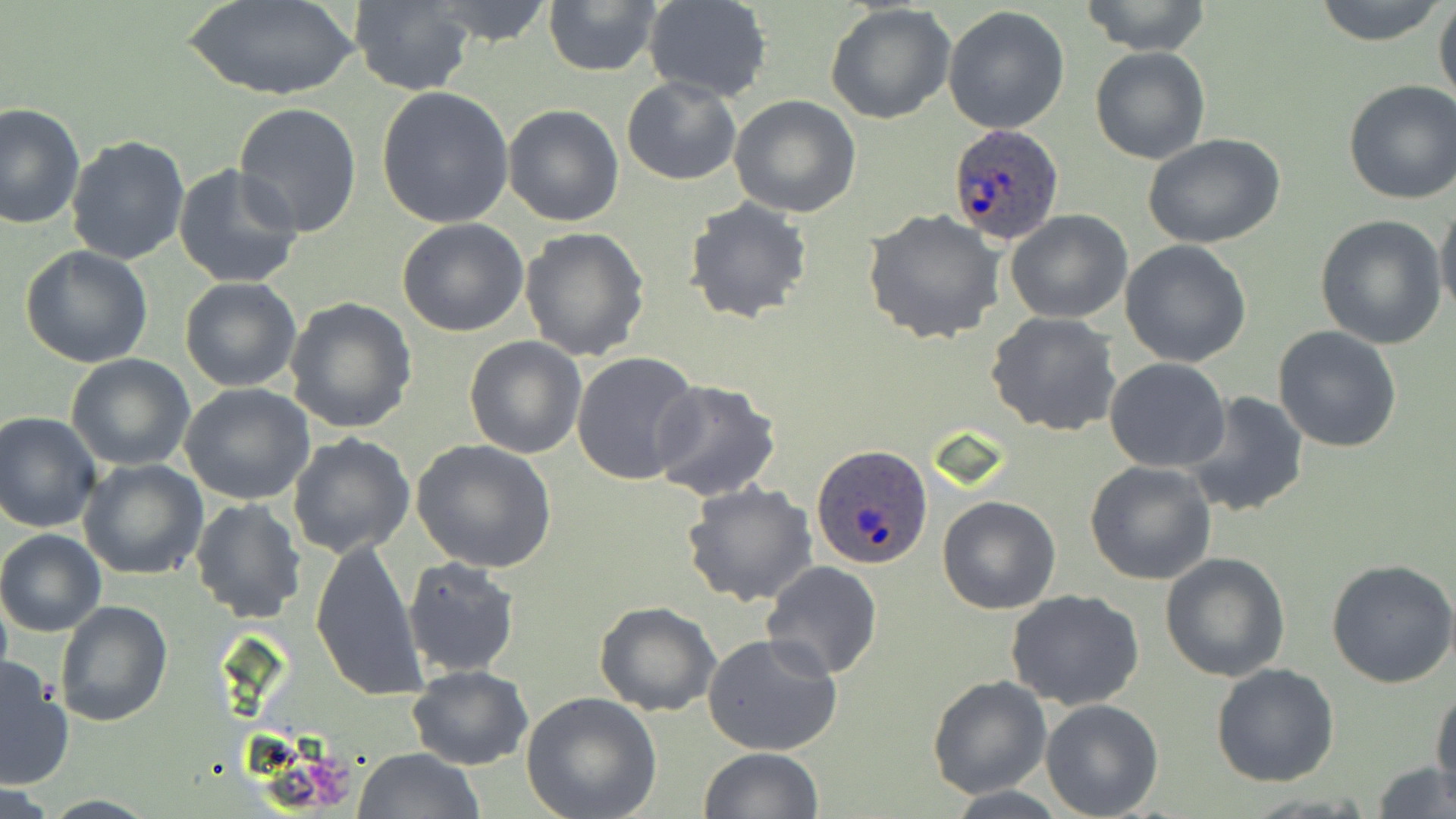 Approximate bounding boxes as named x1/y1/x2/y2 corners in pixels. Uninfected red blood cell locations: (x1=184, y1=0, x2=361, y2=102), (x1=424, y1=0, x2=557, y2=46), (x1=543, y1=0, x2=666, y2=76), (x1=644, y1=0, x2=773, y2=103), (x1=1312, y1=0, x2=1446, y2=45), (x1=1080, y1=1, x2=1211, y2=55), (x1=349, y1=2, x2=476, y2=94), (x1=1433, y1=2, x2=1456, y2=116), (x1=826, y1=3, x2=956, y2=125), (x1=943, y1=6, x2=1071, y2=134), (x1=1091, y1=46, x2=1211, y2=164), (x1=622, y1=76, x2=742, y2=186), (x1=1342, y1=80, x2=1456, y2=205), (x1=375, y1=87, x2=515, y2=231), (x1=729, y1=94, x2=861, y2=219), (x1=0, y1=102, x2=85, y2=232), (x1=232, y1=102, x2=363, y2=237), (x1=501, y1=103, x2=625, y2=226), (x1=1142, y1=133, x2=1286, y2=250), (x1=65, y1=134, x2=192, y2=266), (x1=172, y1=165, x2=303, y2=288), (x1=682, y1=198, x2=813, y2=324), (x1=1436, y1=199, x2=1455, y2=321), (x1=863, y1=209, x2=1003, y2=343), (x1=1005, y1=210, x2=1132, y2=325), (x1=1314, y1=216, x2=1448, y2=348), (x1=396, y1=218, x2=529, y2=337), (x1=519, y1=228, x2=651, y2=361), (x1=1120, y1=240, x2=1252, y2=368), (x1=19, y1=245, x2=153, y2=368), (x1=178, y1=277, x2=302, y2=392), (x1=285, y1=296, x2=417, y2=433), (x1=986, y1=310, x2=1122, y2=436), (x1=1272, y1=326, x2=1402, y2=451), (x1=464, y1=336, x2=585, y2=459), (x1=572, y1=350, x2=702, y2=487), (x1=66, y1=354, x2=196, y2=471), (x1=1105, y1=358, x2=1232, y2=472), (x1=648, y1=380, x2=781, y2=502), (x1=179, y1=383, x2=315, y2=504), (x1=1182, y1=391, x2=1309, y2=519), (x1=0, y1=412, x2=101, y2=533), (x1=287, y1=433, x2=416, y2=559), (x1=412, y1=440, x2=556, y2=574), (x1=78, y1=458, x2=207, y2=579), (x1=1085, y1=461, x2=1217, y2=586), (x1=681, y1=482, x2=820, y2=607), (x1=937, y1=495, x2=1060, y2=614), (x1=190, y1=499, x2=305, y2=621), (x1=0, y1=529, x2=105, y2=637), (x1=310, y1=540, x2=426, y2=701), (x1=1160, y1=553, x2=1292, y2=682), (x1=402, y1=557, x2=520, y2=679), (x1=1327, y1=557, x2=1456, y2=687), (x1=760, y1=560, x2=885, y2=679), (x1=1006, y1=591, x2=1146, y2=711), (x1=54, y1=600, x2=173, y2=727), (x1=596, y1=602, x2=720, y2=716), (x1=701, y1=632, x2=843, y2=755), (x1=0, y1=656, x2=74, y2=790), (x1=1211, y1=663, x2=1341, y2=787), (x1=407, y1=665, x2=534, y2=770), (x1=926, y1=675, x2=1051, y2=799), (x1=1432, y1=688, x2=1455, y2=798), (x1=520, y1=692, x2=663, y2=819), (x1=1040, y1=700, x2=1165, y2=818), (x1=354, y1=748, x2=483, y2=819), (x1=697, y1=748, x2=823, y2=819), (x1=1369, y1=762, x2=1453, y2=818). Plasmodium ovale-infected red blood cell locations: (x1=946, y1=123, x2=1064, y2=244), (x1=811, y1=444, x2=934, y2=572). Slide-level diagnosis: Plasmodium ovale. Single field of view. 1000x magnification. May-Grünwald-Giemsa stain. Thin blood film. Optical microscopy. Image is 1456×819 pixels.